Identify the cell.
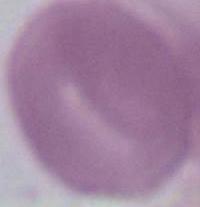
This is an erythrocyte.

{
  "modality": "photomicrograph",
  "magnification": "1000x"
}